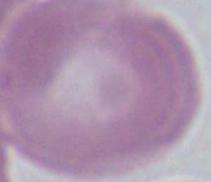

Summary:
  - Magnification: 1000x
  - Modality: micrograph
  - Identification: erythrocyte